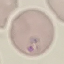
malaria_status: parasitized
preparation: thin blood film
capture: smartphone camera at the microscope eyepiece
stain: Giemsa
image_type: automatically extracted cell patch, resized to 64 × 64 pixels